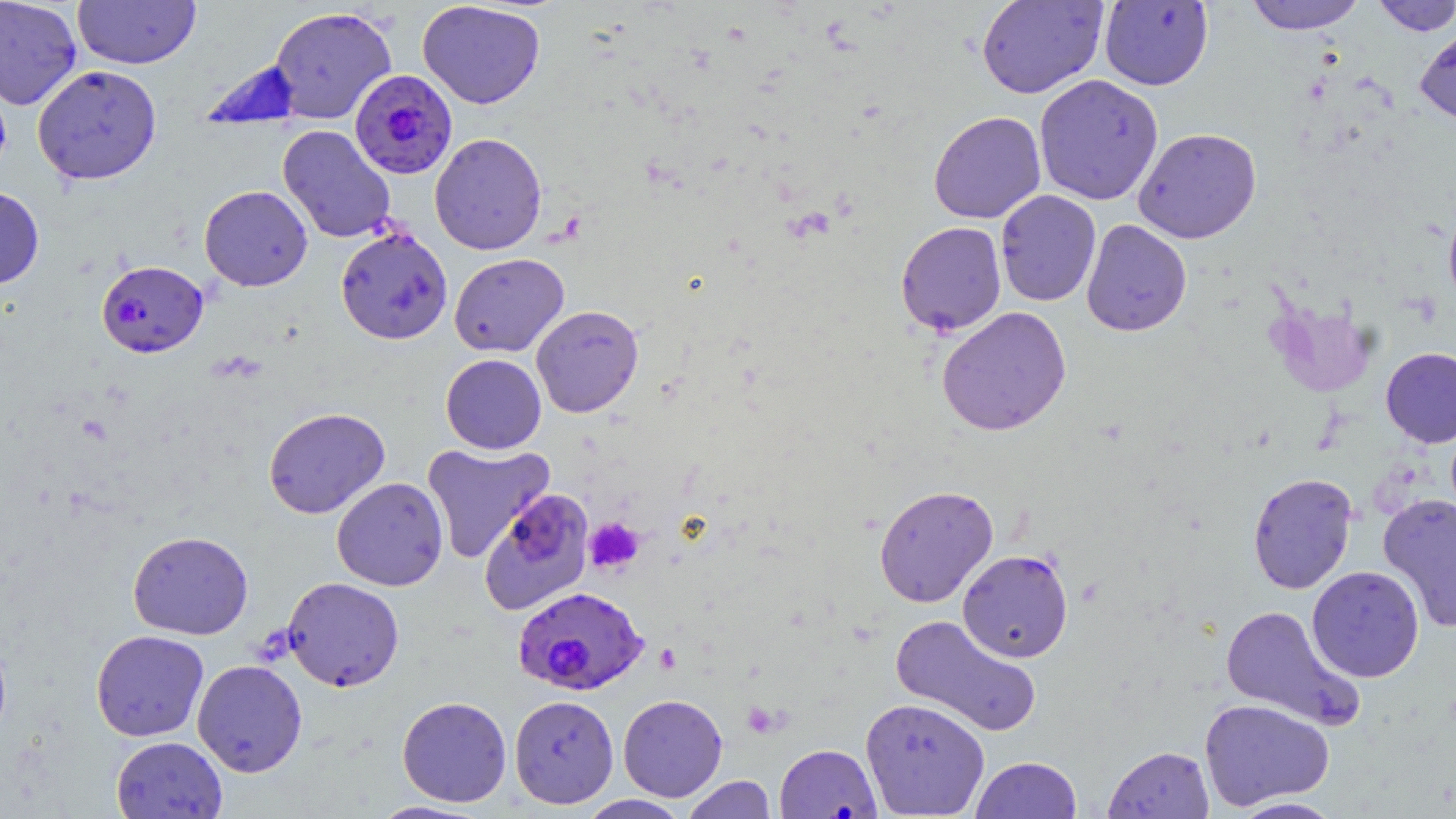
{
  "slide_level_diagnosis": "Plasmodium falciparum",
  "preparation": "thin blood film",
  "platelet_locations": "approximate bounding boxes as (x1, y1, x2, y2) in pixels: (584, 517, 644, 574)",
  "field_of_view": "one of a larger specimen",
  "stain": "May-Grünwald-Giemsa",
  "image_size": "1456×819 pixels",
  "magnification": "1000x",
  "plasmodium_falciparum_infected_red_blood_cell_locations": "approximate bounding boxes as (x1, y1, x2, y2) in pixels: (349, 69, 457, 179), (96, 260, 209, 357), (511, 586, 649, 694)",
  "modality": "light microscopy",
  "uninfected_red_blood_cell_locations": "approximate bounding boxes as (x1, y1, x2, y2) in pixels: (0, 0, 83, 110), (73, 0, 201, 69), (975, 0, 1107, 99), (1244, 0, 1367, 34), (417, 1, 546, 109), (1099, 1, 1214, 90), (1372, 1, 1456, 35), (269, 6, 397, 124), (1415, 22, 1456, 131), (32, 64, 162, 185), (1034, 74, 1164, 206), (928, 111, 1046, 224), (277, 125, 396, 243), (1133, 127, 1261, 243), (429, 132, 547, 255), (199, 185, 313, 291), (0, 186, 45, 289), (996, 190, 1101, 307), (1443, 196, 1456, 314), (1081, 219, 1192, 336), (895, 221, 1007, 336), (335, 226, 453, 345), (449, 253, 569, 357), (531, 305, 644, 417), (936, 306, 1072, 437), (1380, 347, 1456, 448), (440, 354, 546, 454), (263, 407, 390, 519), (421, 442, 555, 563), (1247, 472, 1358, 594), (331, 477, 448, 591), (873, 484, 999, 607), (479, 489, 596, 617), (1378, 493, 1456, 634), (128, 531, 254, 640), (957, 549, 1074, 663), (1307, 565, 1425, 683), (282, 576, 404, 692), (1219, 604, 1362, 729), (890, 614, 1042, 737), (0, 628, 12, 748), (90, 630, 209, 741), (192, 659, 308, 777), (618, 694, 727, 802), (509, 695, 619, 809), (397, 696, 512, 807), (860, 697, 989, 817), (1199, 698, 1335, 810), (111, 735, 227, 819), (1103, 745, 1214, 818), (772, 749, 878, 819), (970, 756, 1082, 818), (682, 775, 777, 819), (577, 795, 693, 819), (1229, 796, 1345, 818), (367, 800, 490, 818)"
}